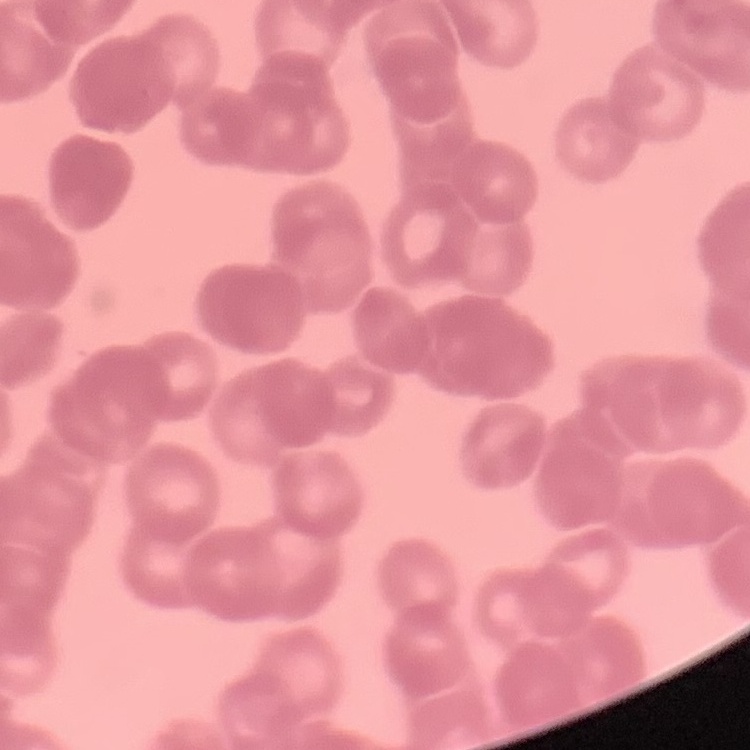

The erythrocytes show rouleaux formation. Thin blood smear. Field's or Giemsa stain. Square crop of a larger photomicrograph.